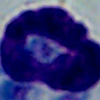
A white blood cell is seen. 1000x magnification. Micrograph.